Report the malaria status of this cell.
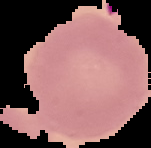

Uninfected.

The area outside the segmented cell region is set to black. From a thin blood film. Image is 151×148 pixels.